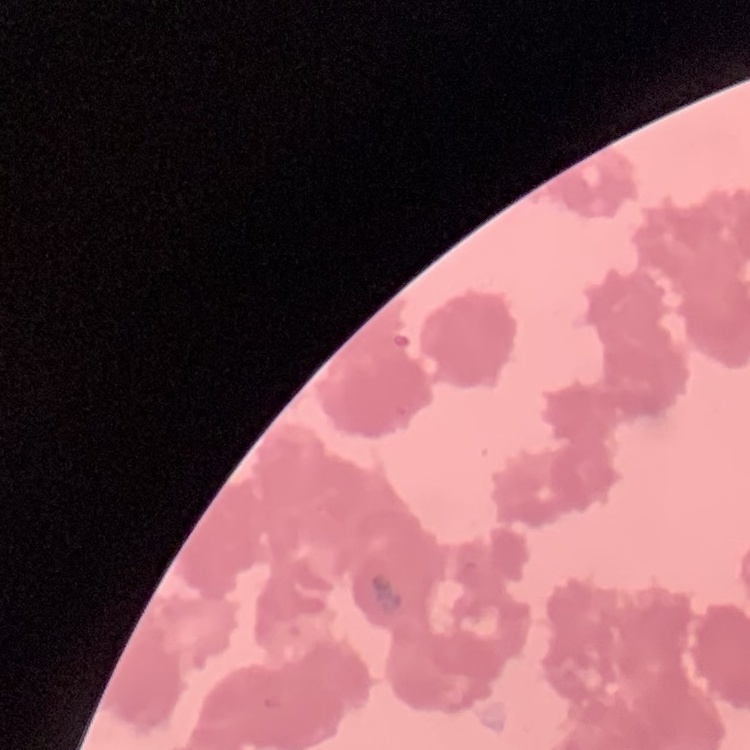
The red blood cells show rouleaux formation. Thin blood film. Field's or Giemsa stain. Square crop of a larger photomicrograph.